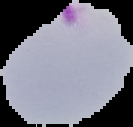
image size = 133×127 pixels
image type = cell region segmented out of the field of view; surrounding area masked to black
malaria status = parasitized
preparation = thin blood film